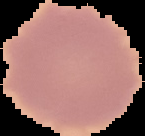

Summary:
  - Malaria status: uninfected
  - Image size: 145×136 pixels
  - Image type: cell region segmented out of the field of view; surrounding area masked to black
  - Preparation: thin blood film